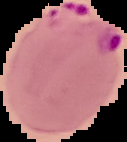
result = malaria parasites detected
image type = segmented cell region on a black background
image size = 127×142 pixels
preparation = thin blood film